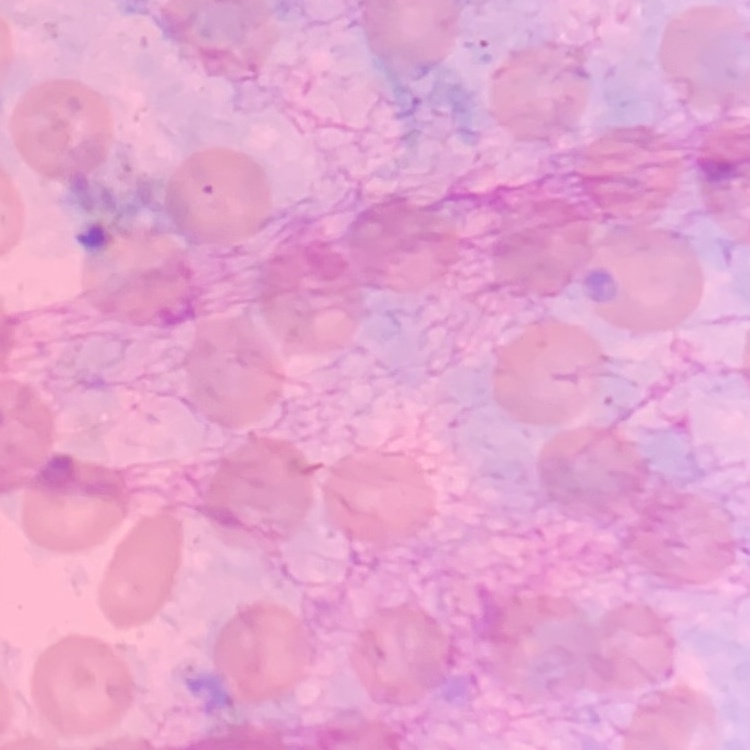

The erythrocytes show no rouleaux formation. Stained with either Field's or Giemsa. Thin peripheral smear. One tile cut from a larger photomicrograph.